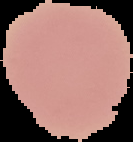

Summary:
  - Image type: segmented cell region with the area outside set to black
  - Malaria status: uninfected
  - Preparation: thin blood smear
  - Image size: 133×142 pixels